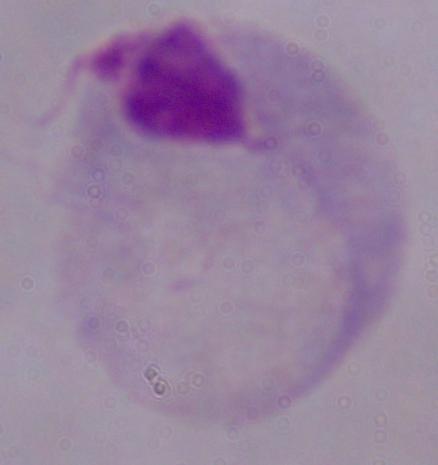

Summary:
  - Magnification: 1000x
  - Identification: trichomonad
  - Modality: micrograph